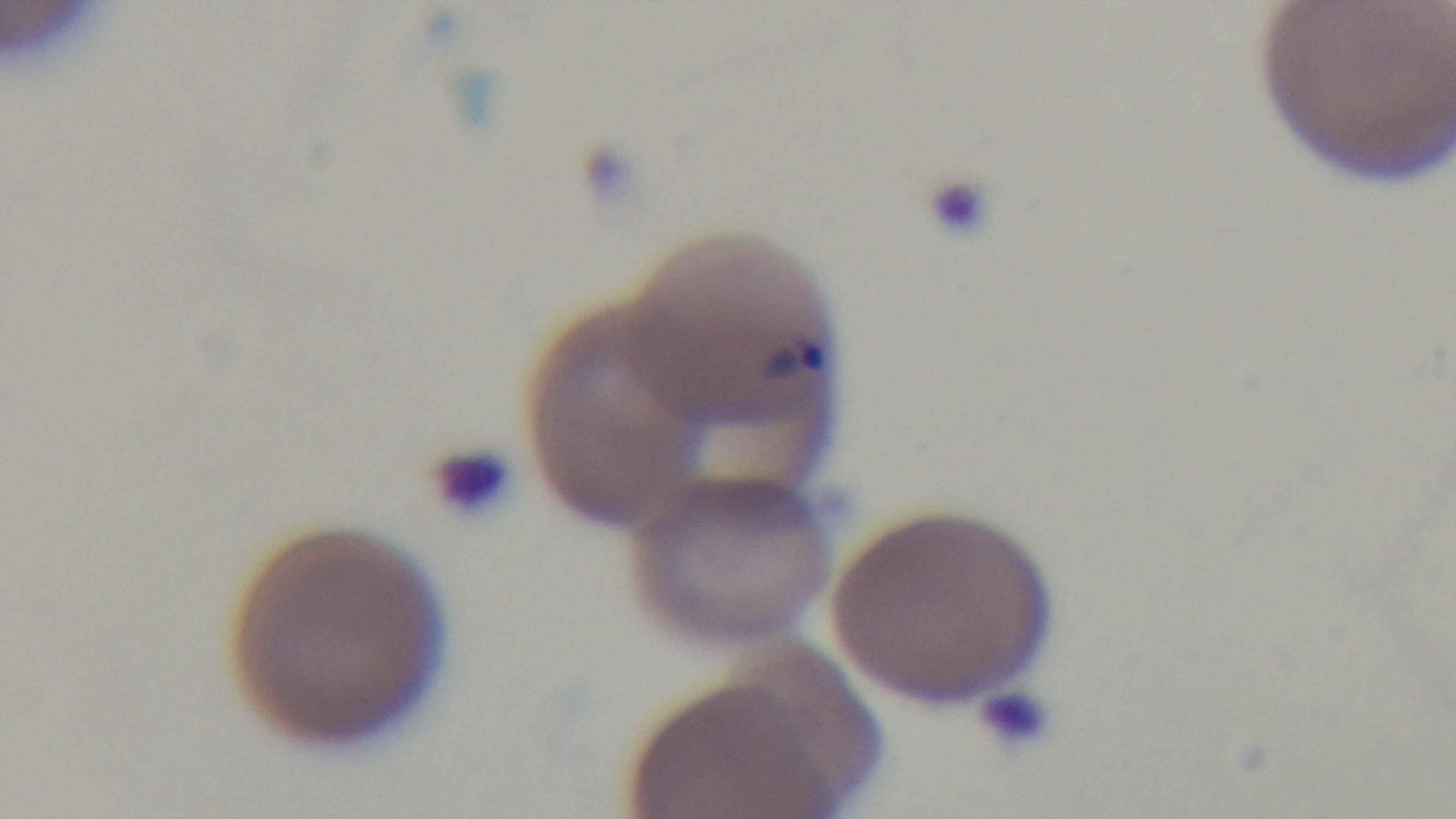

stain: Giemsa
malaria_status: infected
capture: mounted 4K digital camera
modality: light microscopy
objective: 100x oil immersion
preparation: thin
field_of_view: single